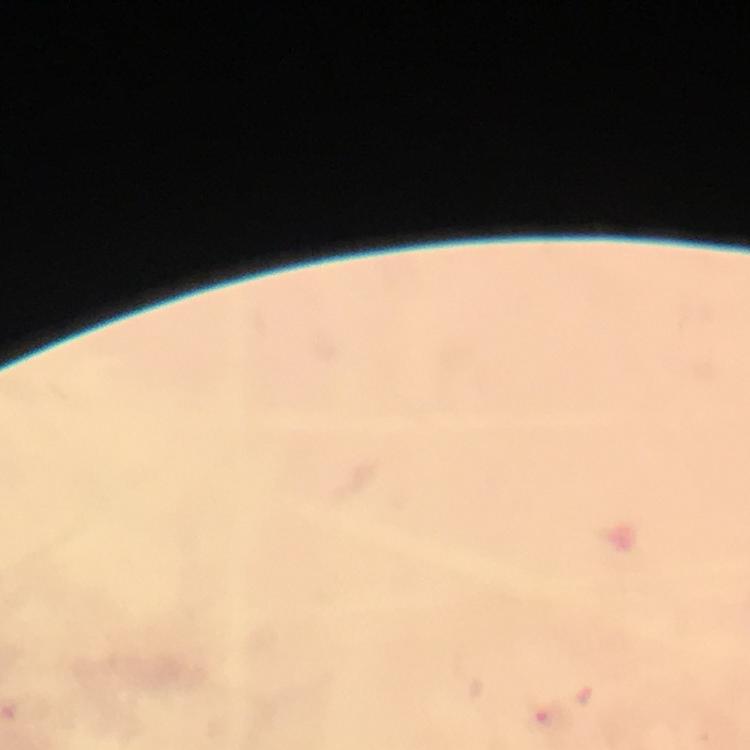
Approximate centers as (x, y) in pixels.
Summary:
  - Plasmodium parasite locations: (549, 719)
  - Capture: smartphone camera through the microscope
  - Immersion oil: used
  - Context: from a malaria diagnostic workup
  - Magnification: 100x
  - Image size: 750×750 pixels
  - Cropped from: a single field of view
  - Stain: Giemsa
  - Preparation: thick blood smear